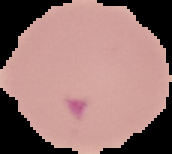

From a thin blood film. Image is 172×154 pixels. Malaria status: parasitized. The area outside the segmented cell region is set to black.